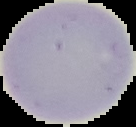
preparation = thin blood film
result = negative for malaria parasites
image type = cell region segmented out of the field of view; surrounding area masked to black
image size = 136×127 pixels